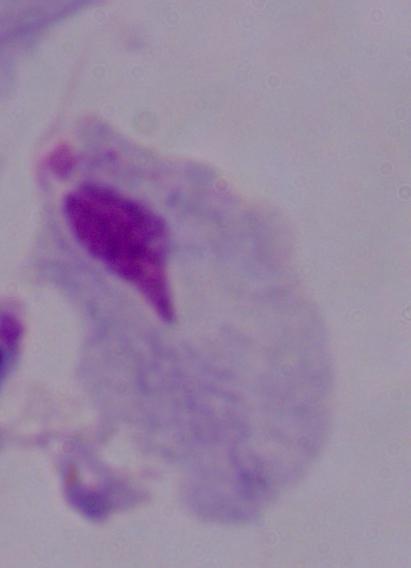

Summary:
  - Modality: photomicrograph
  - Magnification: 1000x
  - Identification: trichomonad